Assess the morphology of the erythrocytes.
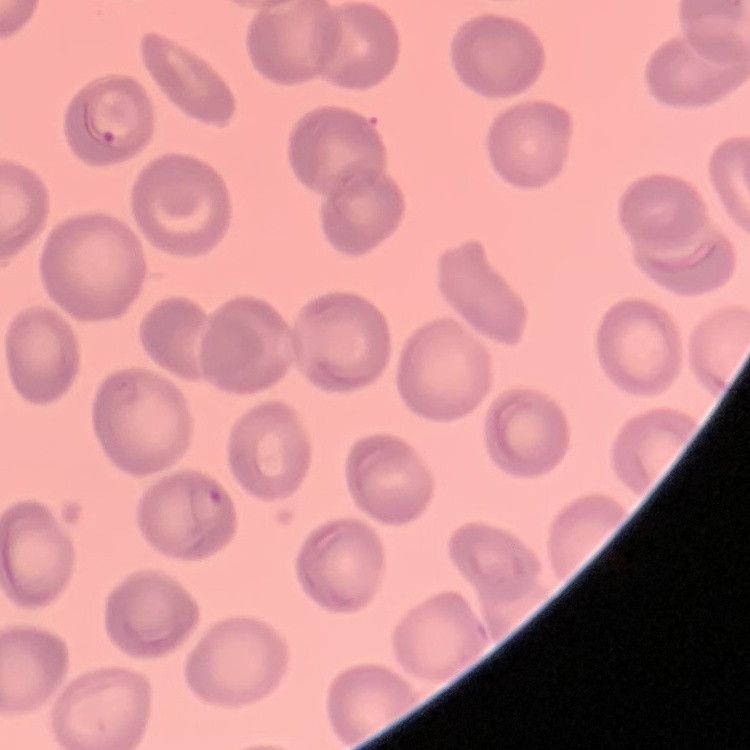

No rouleaux formation.

Thin blood film. Field's or Giemsa stain. One tile cut from a larger photomicrograph.